Look for Plasmodium parasites.
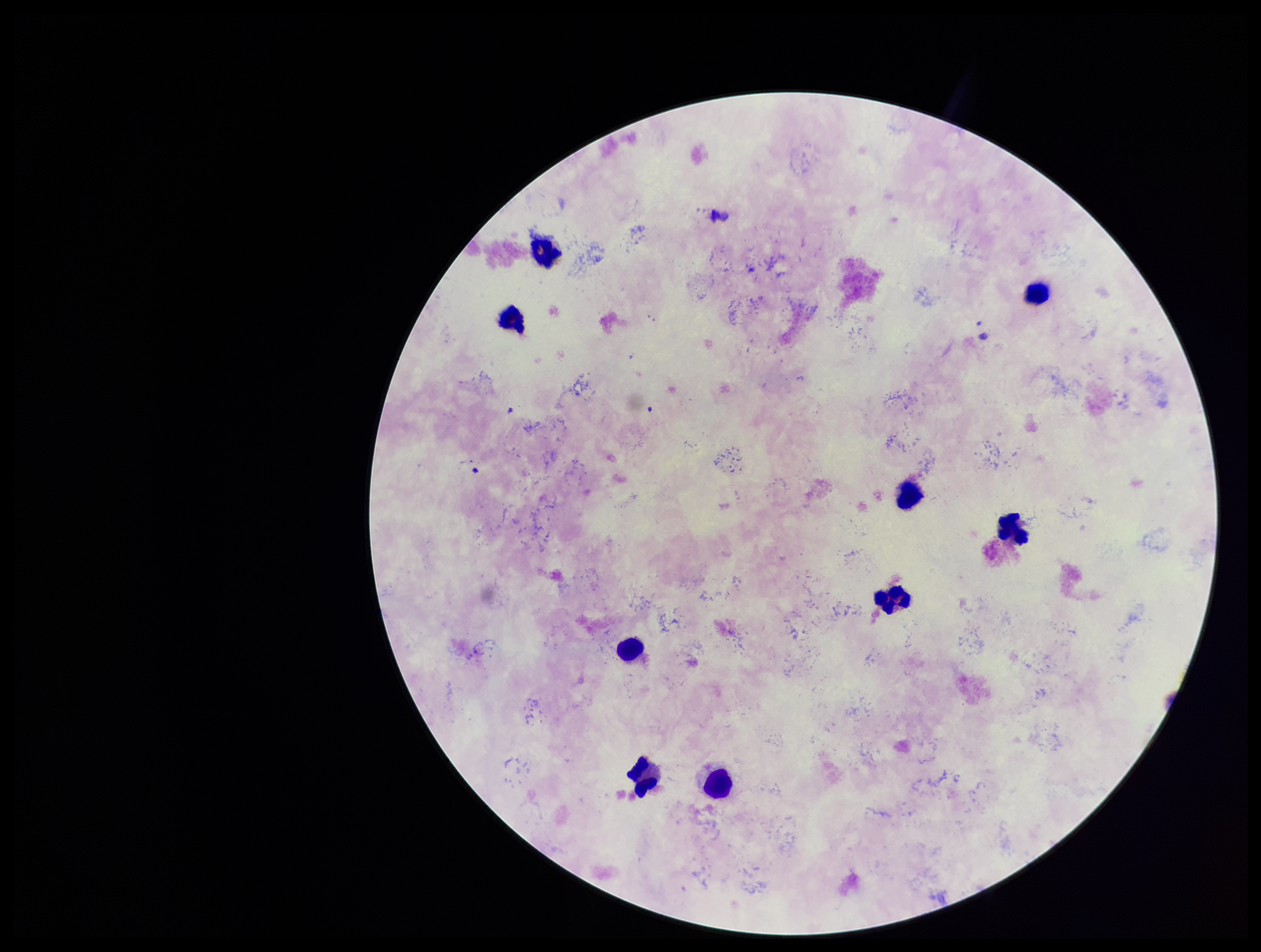

None detected.

Preparation: thick. Patient malaria status: positive. Species reported for this patient: Plasmodium falciparum. Giemsa stain. Parasite count: 0. Photographed through the microscope eyepiece with a smartphone camera. Image is 1261×952 pixels. Leukocyte count: 9. Single field of view.